State which parasite is depicted.
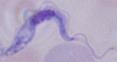
This is a trypanosome.

Micrograph. 1000x magnification.